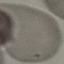 Malaria status: uninfected. Automatically extracted cell patch, resized to 64 × 64 pixels. Photographed with a smartphone camera at the microscope eyepiece. Thin blood film. Giemsa stain.